Assess this cell for malaria.
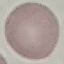

It is uninfected.

preparation = thin blood film
stain = Giemsa
capture = smartphone through the microscope eyepiece
image type = automatically extracted cell patch, resized to 64 × 64 pixels